Point out each leukocyte.
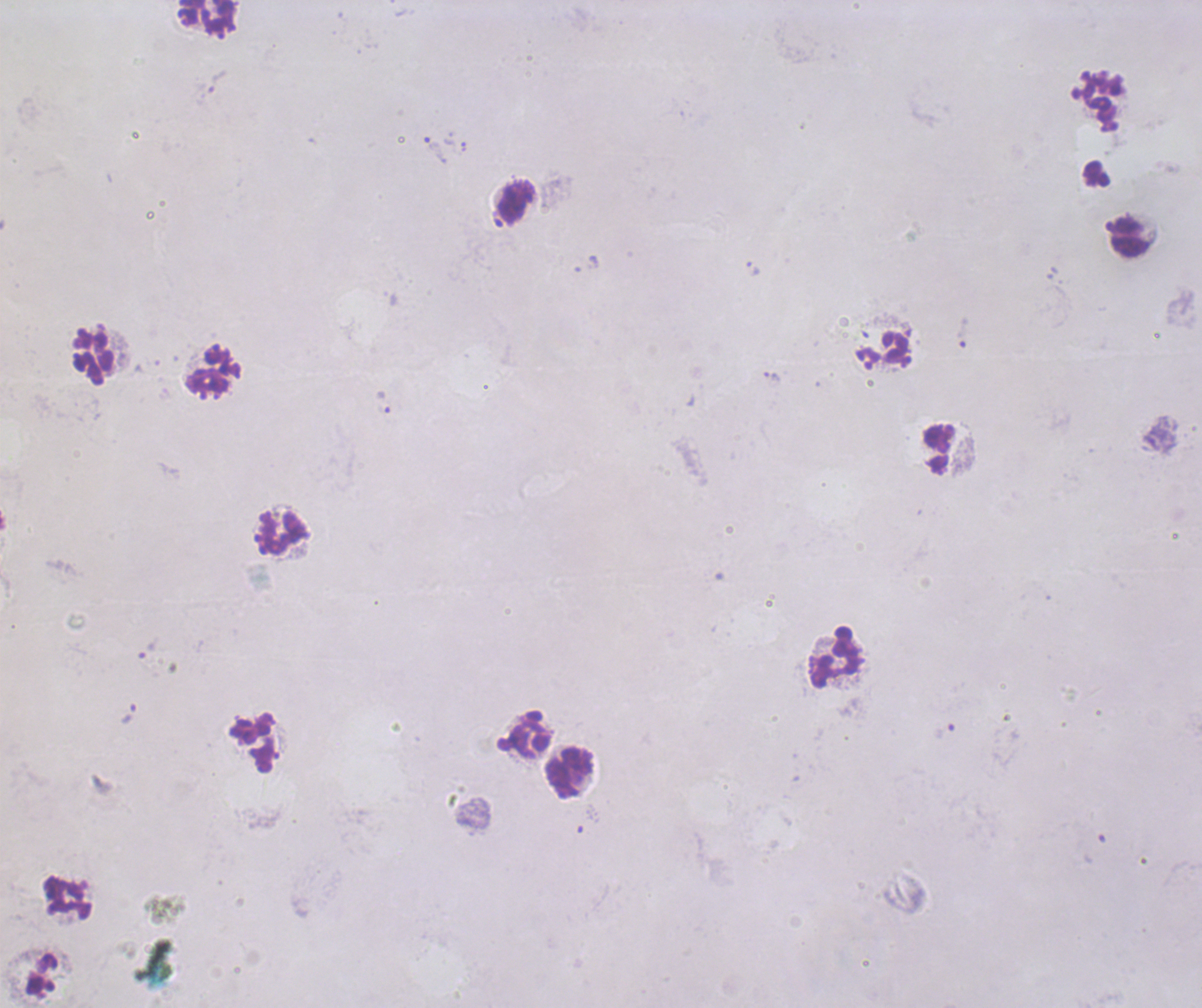

Approximate centers as (x, y) in pixels.
Leukocytes: (206, 18), (517, 200), (1130, 236), (94, 356), (213, 371), (939, 450), (283, 532), (834, 658), (526, 734), (253, 744), (569, 773), (68, 899).

field_of_view: single
magnification: 100x
context: previously used in an actual diagnosis
image_size: 1202×1008 pixels
trophozoite_locations: 'approximate centers as (x, y) in pixels: (436, 150), (753, 269), (963, 332), (773, 376), (382, 403), (129, 714), (944, 731)'
result: Plasmodium parasites identified
preparation: thick blood film
stain: Romanowsky
background_quality: poor
coloration_quality: bad